Give the preparation type.
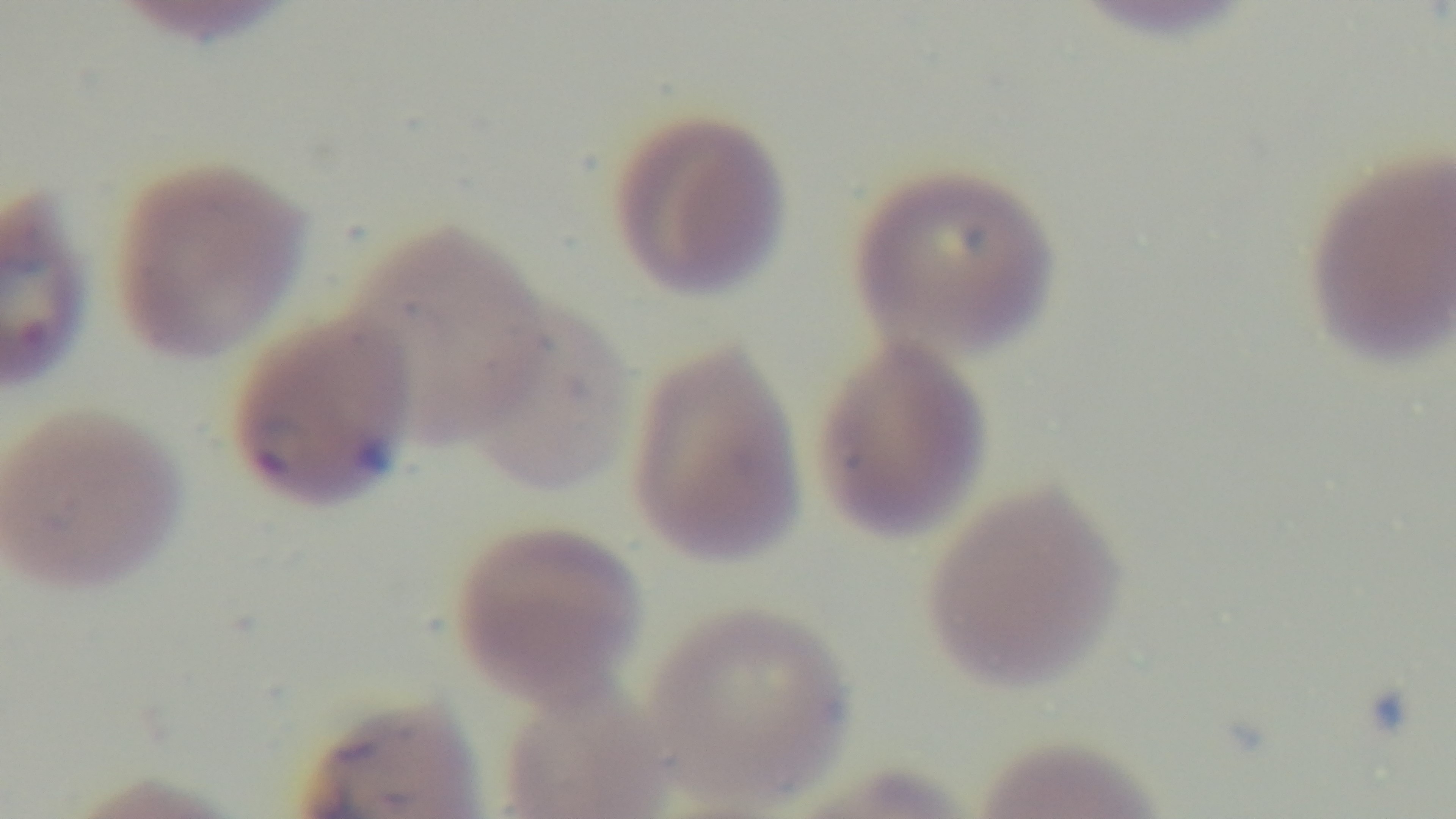

Thin.

Oil-immersion objective, 100x. Malaria status: positive. Single field of view. Photomicrograph. Giemsa-stained. Mounted 4K digital camera.